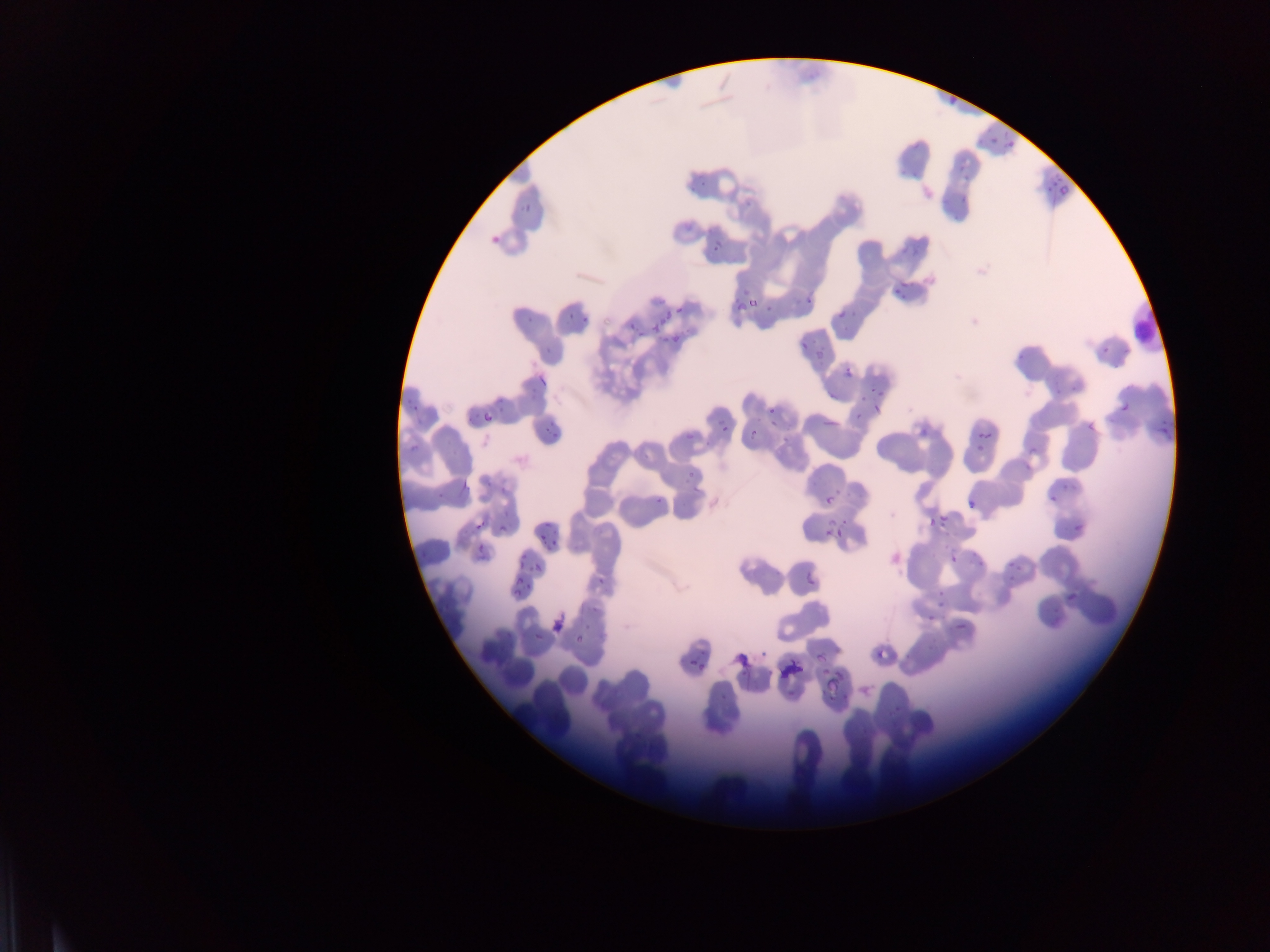

Approximate bounding boxes as [left, top, right, bottom] in pixels. Malaria parasite locations: [945, 92, 956, 105], [1004, 129, 1017, 139], [990, 137, 998, 145], [1001, 143, 1014, 152], [1055, 186, 1069, 201], [959, 191, 967, 201], [518, 200, 539, 212], [490, 229, 501, 242], [714, 244, 723, 253], [898, 287, 915, 304], [806, 292, 816, 304], [749, 293, 759, 313], [761, 294, 785, 317], [737, 300, 748, 311], [652, 306, 671, 334], [675, 306, 684, 315], [835, 306, 850, 323], [566, 309, 594, 325], [524, 312, 542, 327], [629, 322, 642, 338], [665, 328, 691, 340], [798, 341, 808, 350], [1095, 341, 1116, 364], [809, 347, 833, 363], [844, 366, 853, 377], [1039, 370, 1074, 402], [536, 374, 546, 384], [868, 386, 888, 400], [498, 391, 511, 419], [403, 392, 432, 424], [856, 396, 866, 400], [1120, 401, 1131, 415], [874, 403, 883, 412], [767, 407, 776, 415], [545, 409, 570, 435], [848, 410, 866, 427], [484, 412, 492, 421], [1147, 418, 1173, 439], [719, 419, 729, 439], [1084, 419, 1099, 435], [825, 420, 837, 430], [916, 423, 936, 436], [686, 428, 696, 439], [749, 429, 758, 437], [979, 430, 989, 440], [406, 437, 423, 456], [973, 441, 987, 454], [1026, 447, 1043, 454], [685, 467, 697, 480], [441, 480, 454, 496], [1058, 484, 1071, 490], [834, 487, 848, 500], [651, 492, 668, 504], [823, 495, 832, 505], [1048, 495, 1059, 508], [966, 499, 975, 511], [502, 507, 517, 531], [836, 513, 851, 529], [933, 513, 947, 527], [819, 516, 839, 531], [922, 517, 938, 530], [534, 518, 553, 532], [475, 520, 487, 532], [1072, 522, 1086, 532], [833, 525, 842, 544], [539, 531, 554, 547], [823, 531, 832, 540], [474, 540, 491, 561], [966, 550, 990, 568], [510, 551, 534, 572], [1001, 552, 1025, 586], [892, 553, 902, 564], [950, 554, 959, 564], [533, 563, 543, 575], [587, 573, 610, 586], [808, 577, 817, 588], [513, 581, 525, 595], [933, 586, 949, 599], [1064, 587, 1084, 605], [937, 601, 947, 607], [1049, 605, 1063, 623], [921, 613, 939, 625], [573, 620, 594, 657], [953, 622, 974, 639], [533, 633, 541, 642], [813, 636, 845, 663], [755, 637, 770, 665], [686, 645, 707, 670], [876, 647, 887, 664], [736, 652, 749, 666], [792, 662, 803, 673], [776, 664, 794, 685], [824, 670, 847, 699] | approximate [x, y] pixel centers of objects too small to bound: [968, 172]. Leukocyte locations: [1123, 297, 1169, 355]. Sample from Ghana. Image is 1270×952 pixels. Thin blood film. Photographed through a microscope with a mobile-phone camera. One field of view.